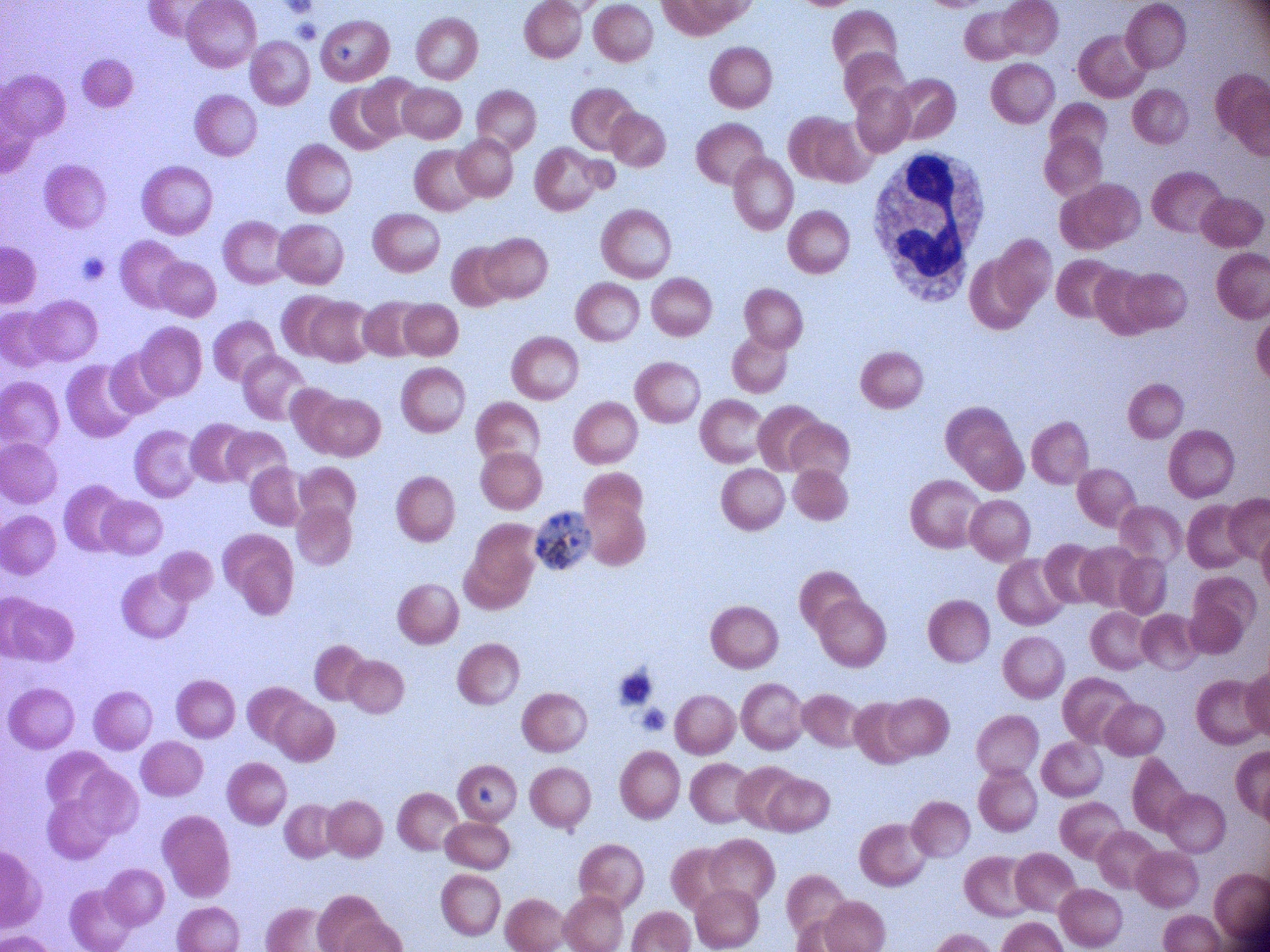

Approximate bounding boxes as (x1, y1, x2, y2) in pixels, from the source annotation, which is not necessarily exhaustive.
Summary:
  - Schizont locations: (536, 514, 590, 571)
  - Stain: Giemsa
  - Microscope: Leica DM2000 with built-in camera
  - Preparation: thin blood film
  - Magnification: 100x
  - Field of view: one from this slide
  - Species: Plasmodium falciparum
  - Image size: 1270×952 pixels